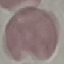
Summary:
  - Result: no malaria parasites seen
  - Image type: automatically extracted cell patch, resized to 64 × 64 pixels
  - Capture: smartphone through the microscope eyepiece
  - Preparation: thin smear
  - Stain: Giemsa